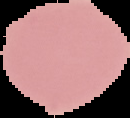
Summary:
  - Malaria status: uninfected
  - Preparation: thin blood smear
  - Image type: segmented cell region on a black background
  - Image size: 130×118 pixels